Comment on the morphology of the red blood cells.
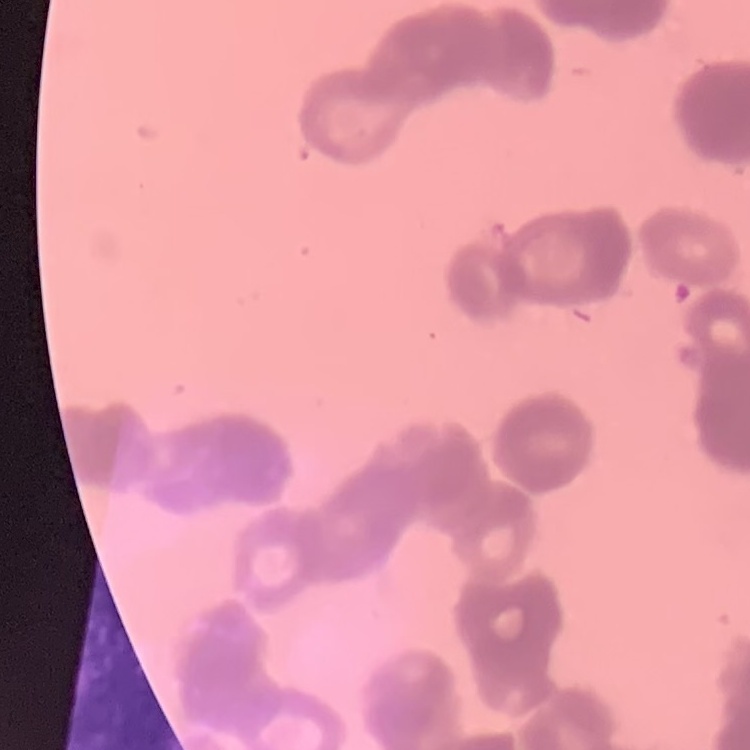
They show rouleaux formation.

Summary:
  - Image type: one tile cut from a larger photomicrograph
  - Preparation: thin blood film
  - Stain: Field's or Giemsa